Outline each blood parasite and name the species.
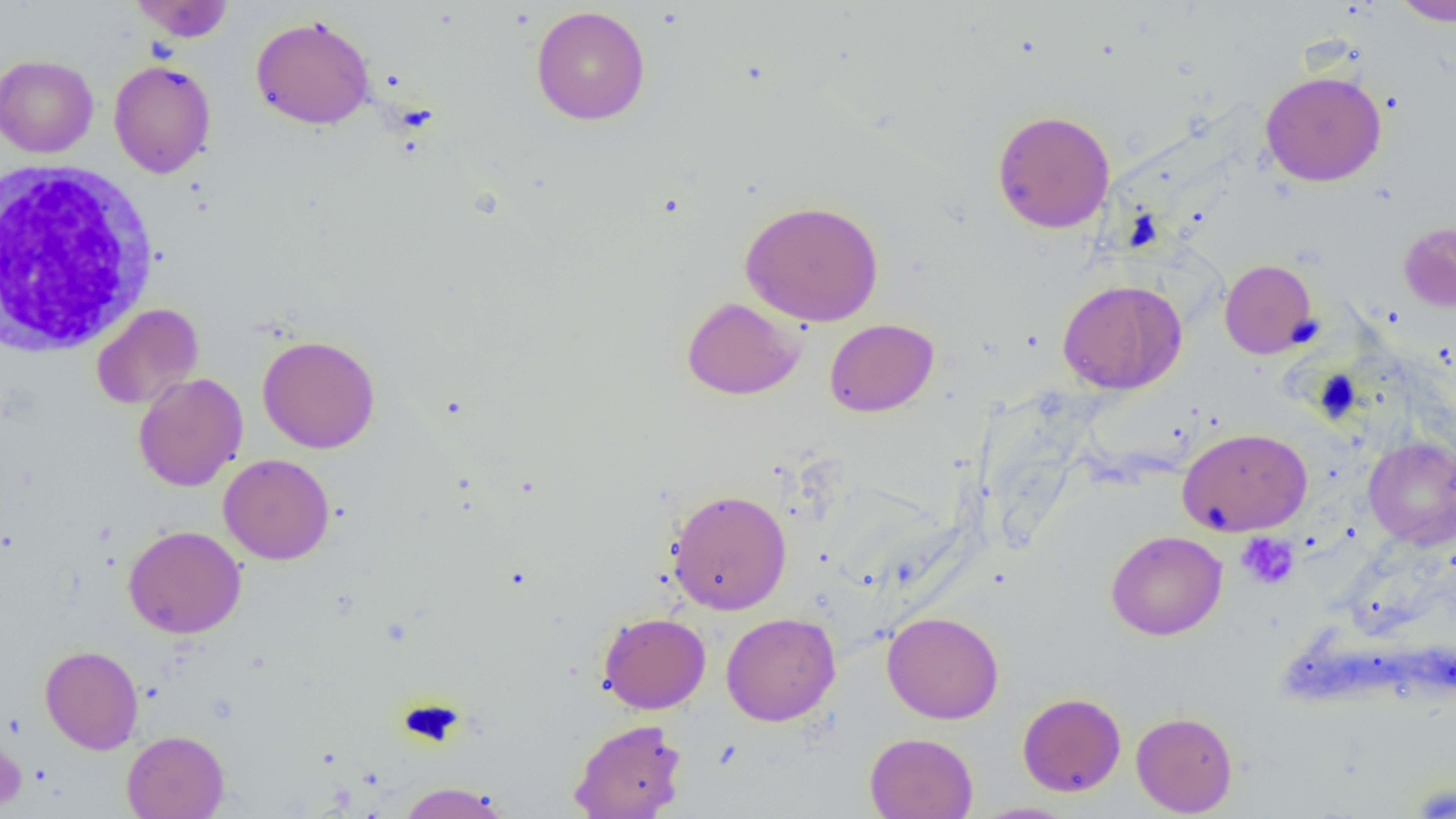

No blood parasites observed.

Summary:
  - Coordinate format: approximate bounding boxes as (x1,y1)-(x2,y2) corner pairs in pixels
  - White blood cell locations: (0,158)-(159,356)
  - Platelet locations: (1236,532)-(1299,589)
  - Uninfected red blood cell locations: (130,0)-(234,42), (1390,0)-(1456,26), (531,6)-(650,125), (251,15)-(376,130), (0,55)-(99,158), (109,59)-(216,178), (1260,70)-(1387,186), (992,109)-(1115,234), (740,200)-(884,326), (1398,221)-(1456,313), (1219,259)-(1319,359), (1058,280)-(1187,394), (681,297)-(805,400), (91,303)-(204,409), (824,318)-(939,417), (257,335)-(380,453), (133,373)-(248,492), (1178,427)-(1311,536), (1363,436)-(1456,549), (219,454)-(335,565), (666,488)-(792,615), (123,525)-(247,639), (1106,530)-(1227,640), (882,611)-(1004,724), (598,612)-(711,714), (721,612)-(840,726), (39,645)-(143,754), (1017,692)-(1126,796), (1131,711)-(1238,817), (568,718)-(686,819), (0,724)-(27,814), (122,730)-(229,819), (865,732)-(978,819), (395,782)-(514,818), (971,802)-(1079,819)
  - Slide-level diagnosis: negative for blood parasites
  - Preparation: thin blood smear
  - Modality: optical microscopy
  - Field of view: one of a larger specimen
  - Magnification: 1000x
  - Image size: 1456×819 pixels